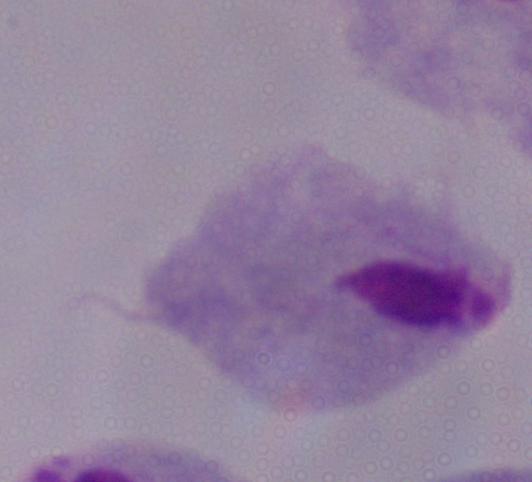

modality = micrograph
identification = trichomonad
magnification = 1000x